Report the malaria status of this cell.
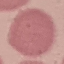
Uninfected.

capture: smartphone camera at the microscope eyepiece
stain: Giemsa
image_type: automatically extracted cell patch, resized to 64 × 64 pixels
preparation: thin blood smear